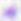
Toxoplasma gondii is seen. Micrograph. Captured at 400x magnification.